Classify this cell by malaria status.
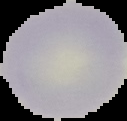

Uninfected.

image size = 127×121 pixels
image type = cell region segmented out of the field of view; surrounding area masked to black
preparation = thin blood smear